Identify the cell.
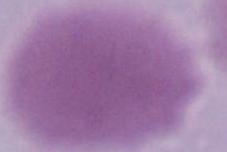
This is an erythrocyte.

1000x magnification. Micrograph.